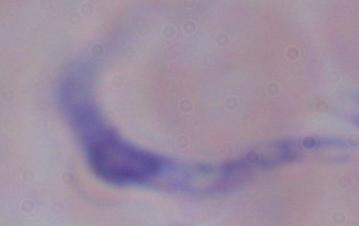

Summary:
  - Identification: trypanosome
  - Modality: micrograph
  - Magnification: 1000x